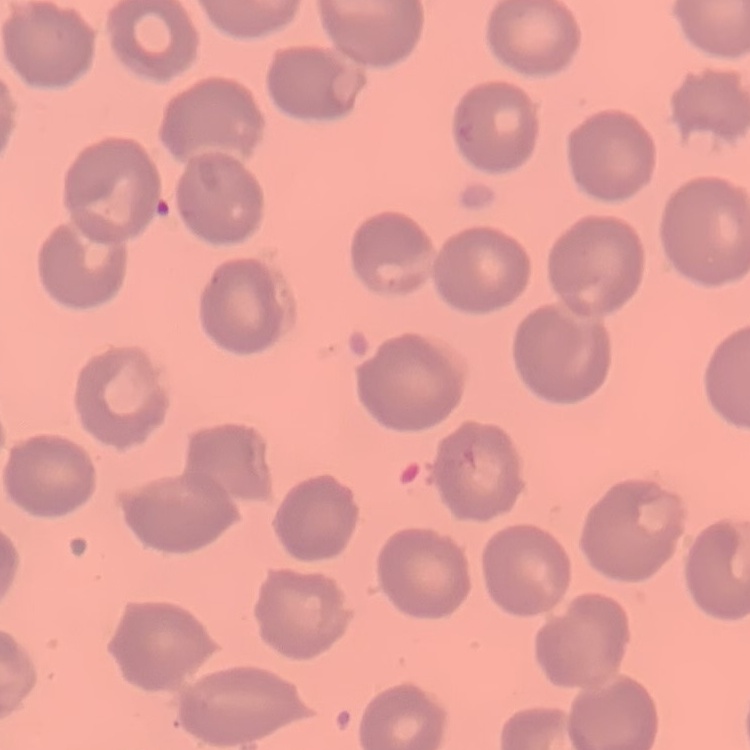

red blood cell morphology = no rouleaux formation
image type = one tile cut from a larger photomicrograph
stain = Field's or Giemsa
preparation = thin peripheral smear